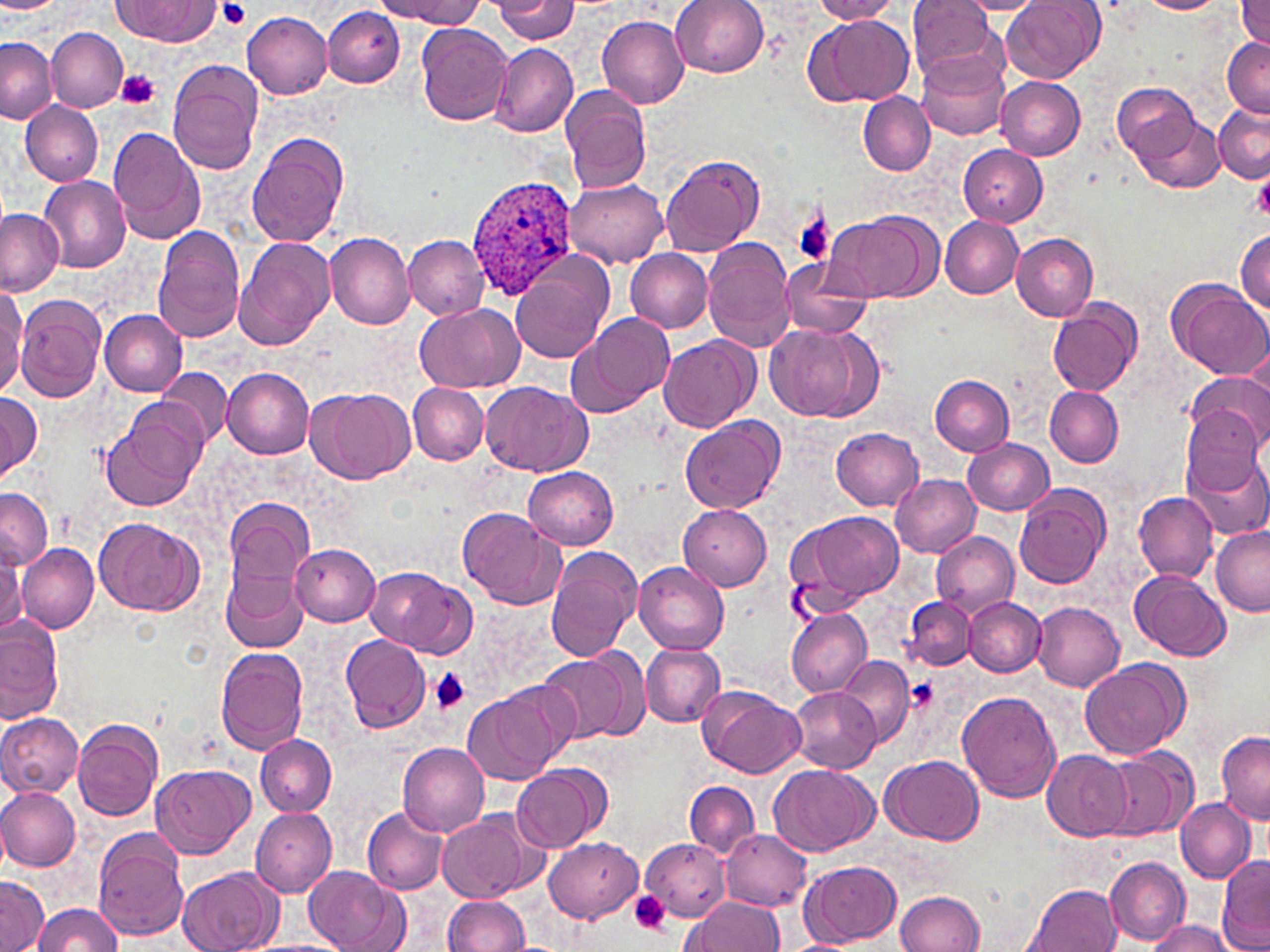
Summary:
  - Coordinate format: approximate bounding boxes as named x1/y1/x2/y2 corners in pixels
  - Plasmodium ovale-infected red blood cell locations: (x1=465, y1=173, x2=578, y2=294)
  - Uninfected red blood cell locations: (x1=377, y1=0, x2=482, y2=27), (x1=492, y1=0, x2=581, y2=42), (x1=672, y1=0, x2=769, y2=77), (x1=809, y1=0, x2=903, y2=22), (x1=907, y1=0, x2=1003, y2=83), (x1=1001, y1=0, x2=1104, y2=84), (x1=1235, y1=0, x2=1270, y2=47), (x1=117, y1=1, x2=219, y2=43), (x1=954, y1=1, x2=1049, y2=15), (x1=1137, y1=1, x2=1226, y2=13), (x1=322, y1=7, x2=405, y2=87), (x1=243, y1=12, x2=332, y2=99), (x1=805, y1=13, x2=915, y2=106), (x1=596, y1=14, x2=688, y2=108), (x1=416, y1=23, x2=513, y2=125), (x1=46, y1=28, x2=128, y2=113), (x1=1221, y1=38, x2=1270, y2=116), (x1=1, y1=39, x2=57, y2=122), (x1=490, y1=44, x2=577, y2=137), (x1=916, y1=48, x2=1009, y2=142), (x1=168, y1=59, x2=264, y2=176), (x1=996, y1=77, x2=1086, y2=160), (x1=1112, y1=82, x2=1199, y2=167), (x1=561, y1=86, x2=654, y2=196), (x1=857, y1=93, x2=935, y2=174), (x1=21, y1=100, x2=103, y2=186), (x1=1213, y1=101, x2=1270, y2=183), (x1=1128, y1=111, x2=1225, y2=194), (x1=107, y1=126, x2=207, y2=244), (x1=247, y1=132, x2=350, y2=249), (x1=960, y1=144, x2=1048, y2=225), (x1=660, y1=154, x2=764, y2=256), (x1=1253, y1=164, x2=1270, y2=225), (x1=40, y1=176, x2=131, y2=273), (x1=564, y1=178, x2=668, y2=267), (x1=0, y1=207, x2=65, y2=294), (x1=823, y1=211, x2=939, y2=303), (x1=941, y1=218, x2=1022, y2=298), (x1=151, y1=226, x2=246, y2=342), (x1=1234, y1=231, x2=1269, y2=314), (x1=324, y1=232, x2=416, y2=329), (x1=234, y1=234, x2=336, y2=351), (x1=1011, y1=234, x2=1097, y2=320), (x1=404, y1=236, x2=490, y2=320), (x1=703, y1=238, x2=797, y2=351), (x1=625, y1=250, x2=714, y2=332), (x1=508, y1=251, x2=614, y2=365), (x1=778, y1=257, x2=873, y2=340), (x1=1166, y1=279, x2=1269, y2=379), (x1=0, y1=286, x2=26, y2=396), (x1=17, y1=297, x2=106, y2=401), (x1=1048, y1=300, x2=1143, y2=397), (x1=411, y1=302, x2=524, y2=391), (x1=100, y1=310, x2=188, y2=395), (x1=566, y1=313, x2=674, y2=418), (x1=764, y1=323, x2=884, y2=423), (x1=657, y1=336, x2=760, y2=433), (x1=157, y1=367, x2=231, y2=446), (x1=223, y1=369, x2=315, y2=458), (x1=1187, y1=372, x2=1269, y2=453), (x1=930, y1=374, x2=1015, y2=455), (x1=479, y1=380, x2=592, y2=477), (x1=408, y1=383, x2=489, y2=465), (x1=306, y1=386, x2=413, y2=485), (x1=1045, y1=387, x2=1124, y2=467), (x1=0, y1=394, x2=42, y2=481), (x1=1180, y1=404, x2=1262, y2=495), (x1=101, y1=406, x2=206, y2=512), (x1=679, y1=416, x2=784, y2=514), (x1=832, y1=427, x2=923, y2=510), (x1=962, y1=438, x2=1054, y2=514), (x1=1186, y1=454, x2=1268, y2=538), (x1=523, y1=467, x2=620, y2=549), (x1=890, y1=473, x2=980, y2=556), (x1=1013, y1=484, x2=1111, y2=591), (x1=0, y1=487, x2=51, y2=571), (x1=1134, y1=491, x2=1219, y2=581), (x1=221, y1=496, x2=313, y2=629), (x1=679, y1=505, x2=772, y2=590), (x1=457, y1=508, x2=566, y2=611), (x1=785, y1=509, x2=905, y2=614), (x1=95, y1=517, x2=205, y2=615), (x1=1211, y1=524, x2=1270, y2=614), (x1=931, y1=530, x2=1019, y2=616), (x1=16, y1=542, x2=98, y2=633), (x1=290, y1=543, x2=380, y2=626), (x1=545, y1=545, x2=643, y2=664), (x1=0, y1=548, x2=24, y2=636), (x1=633, y1=561, x2=731, y2=655), (x1=364, y1=565, x2=476, y2=658), (x1=223, y1=567, x2=306, y2=652), (x1=1129, y1=567, x2=1233, y2=661), (x1=903, y1=597, x2=976, y2=673), (x1=965, y1=598, x2=1046, y2=676), (x1=1032, y1=601, x2=1125, y2=691), (x1=787, y1=609, x2=871, y2=697), (x1=0, y1=613, x2=64, y2=724), (x1=340, y1=635, x2=432, y2=734), (x1=639, y1=644, x2=726, y2=727), (x1=216, y1=647, x2=308, y2=755), (x1=536, y1=650, x2=647, y2=745), (x1=837, y1=655, x2=915, y2=749), (x1=1078, y1=658, x2=1189, y2=758), (x1=461, y1=682, x2=574, y2=784), (x1=788, y1=686, x2=883, y2=772), (x1=698, y1=688, x2=808, y2=780), (x1=957, y1=690, x2=1061, y2=804), (x1=0, y1=713, x2=84, y2=797), (x1=73, y1=719, x2=162, y2=821), (x1=1215, y1=731, x2=1270, y2=824), (x1=255, y1=733, x2=335, y2=816), (x1=397, y1=742, x2=491, y2=836), (x1=1101, y1=747, x2=1199, y2=841), (x1=1042, y1=750, x2=1133, y2=841), (x1=880, y1=756, x2=985, y2=845), (x1=151, y1=763, x2=255, y2=859), (x1=511, y1=764, x2=610, y2=853), (x1=769, y1=764, x2=877, y2=857), (x1=668, y1=781, x2=778, y2=910), (x1=684, y1=781, x2=759, y2=859), (x1=1, y1=786, x2=81, y2=870), (x1=1174, y1=796, x2=1256, y2=883), (x1=249, y1=806, x2=337, y2=898), (x1=437, y1=808, x2=546, y2=904), (x1=363, y1=809, x2=448, y2=895), (x1=721, y1=827, x2=812, y2=910), (x1=94, y1=828, x2=189, y2=940), (x1=711, y1=831, x2=865, y2=934), (x1=546, y1=838, x2=642, y2=922), (x1=642, y1=839, x2=730, y2=921), (x1=1217, y1=854, x2=1270, y2=950), (x1=1105, y1=855, x2=1190, y2=944), (x1=800, y1=858, x2=903, y2=946), (x1=304, y1=866, x2=408, y2=952), (x1=178, y1=867, x2=281, y2=952), (x1=0, y1=874, x2=48, y2=952), (x1=1024, y1=883, x2=1122, y2=952), (x1=896, y1=890, x2=985, y2=951), (x1=442, y1=894, x2=530, y2=951), (x1=683, y1=896, x2=784, y2=952), (x1=30, y1=902, x2=125, y2=951), (x1=1145, y1=919, x2=1236, y2=952), (x1=242, y1=940, x2=351, y2=952)
  - Platelet locations: (x1=220, y1=0, x2=249, y2=28), (x1=118, y1=69, x2=160, y2=108), (x1=792, y1=211, x2=836, y2=265), (x1=429, y1=668, x2=471, y2=712), (x1=904, y1=677, x2=942, y2=712), (x1=628, y1=889, x2=672, y2=934)
  - Slide-level diagnosis: Plasmodium ovale
  - Stain: May-Grünwald-Giemsa
  - Modality: optical microscopy
  - Field of view: one of a larger specimen
  - Image size: 1270×952 pixels
  - Preparation: thin blood smear
  - Magnification: 1000x